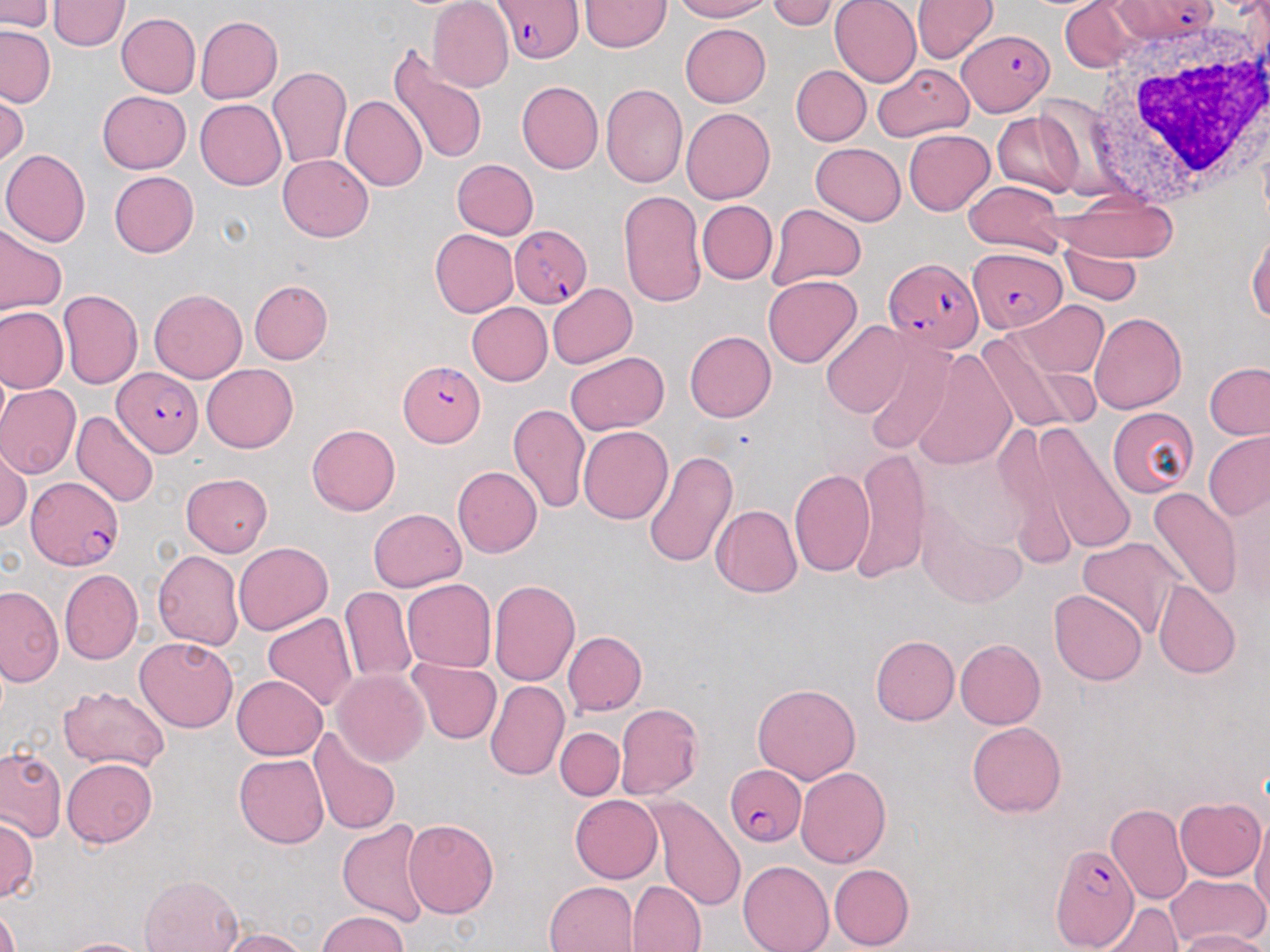
Summary:
  - Coordinate format: approximate bounding boxes as [x1, y1, x2, y2] in pixels
  - Plasmodium falciparum-infected red blood cell locations: [492, 0, 586, 64], [1110, 0, 1219, 42], [958, 29, 1054, 115], [509, 225, 591, 308], [967, 246, 1067, 333], [885, 257, 984, 354], [400, 361, 485, 446], [113, 368, 205, 457], [25, 475, 123, 571], [722, 767, 806, 847], [1049, 845, 1140, 949]
  - White blood cell locations: [1089, 24, 1270, 208]
  - Uninfected red blood cell locations: [428, 0, 513, 92], [579, 0, 669, 52], [671, 0, 775, 21], [767, 0, 838, 30], [830, 0, 922, 87], [911, 0, 999, 63], [1059, 0, 1139, 72], [0, 1, 54, 33], [48, 1, 129, 52], [116, 13, 200, 97], [195, 16, 283, 104], [680, 24, 771, 106], [0, 26, 55, 107], [387, 46, 490, 165], [872, 62, 974, 143], [266, 65, 352, 170], [790, 65, 870, 145], [516, 80, 603, 174], [601, 83, 687, 187], [98, 90, 190, 173], [0, 92, 27, 168], [341, 95, 427, 192], [195, 99, 286, 190], [680, 107, 774, 204], [992, 113, 1082, 196], [904, 129, 995, 215], [811, 143, 905, 225], [1, 150, 91, 247], [278, 154, 373, 242], [452, 159, 539, 239], [109, 171, 199, 258], [964, 181, 1065, 255], [618, 190, 706, 307], [1052, 194, 1176, 262], [697, 200, 777, 284], [767, 203, 867, 289], [0, 225, 66, 316], [1247, 228, 1270, 323], [431, 229, 518, 317], [1062, 244, 1140, 304], [763, 274, 862, 368], [249, 280, 333, 363], [547, 283, 637, 368], [59, 289, 142, 387], [149, 289, 246, 382], [1011, 300, 1107, 378], [467, 303, 553, 386], [0, 306, 68, 393], [1090, 311, 1187, 414], [820, 321, 912, 417], [976, 326, 1094, 437], [685, 331, 777, 422], [859, 334, 956, 455], [912, 348, 1017, 472], [566, 351, 669, 436], [1203, 362, 1270, 440], [201, 364, 298, 453], [0, 385, 81, 479], [507, 403, 590, 514], [1107, 406, 1198, 498], [71, 410, 158, 508], [1022, 421, 1137, 557], [307, 425, 400, 516], [578, 426, 672, 525], [992, 427, 1080, 573], [1203, 431, 1270, 520], [0, 443, 31, 532], [851, 448, 930, 582], [643, 449, 737, 570], [452, 466, 542, 557], [788, 468, 874, 576], [181, 473, 272, 555], [1145, 488, 1242, 602], [914, 498, 1026, 607], [711, 505, 803, 598], [368, 508, 466, 593], [1076, 536, 1187, 641], [233, 542, 332, 634], [152, 549, 244, 650], [59, 568, 142, 665], [402, 578, 497, 673], [489, 580, 579, 686], [1153, 581, 1243, 679], [0, 586, 63, 687], [341, 586, 416, 684], [1049, 589, 1146, 686], [262, 612, 359, 711], [563, 631, 647, 716], [871, 635, 959, 726], [134, 636, 239, 733], [956, 639, 1045, 729], [407, 660, 502, 744], [333, 669, 429, 767], [233, 675, 328, 759], [487, 679, 569, 782], [752, 681, 861, 785], [57, 686, 171, 772], [615, 703, 704, 799], [967, 722, 1066, 818], [309, 727, 401, 834], [555, 727, 624, 799], [0, 746, 65, 841], [234, 754, 329, 848], [62, 758, 157, 847], [796, 768, 892, 868], [570, 795, 663, 883], [644, 796, 748, 913], [1174, 797, 1265, 881], [1106, 804, 1192, 907], [0, 815, 38, 903], [1251, 817, 1270, 920], [403, 818, 499, 918], [337, 819, 431, 927], [738, 860, 834, 952], [829, 863, 914, 951], [1165, 873, 1268, 947], [140, 874, 243, 952], [627, 880, 707, 952], [544, 881, 638, 952], [0, 900, 20, 952], [1097, 901, 1182, 952], [316, 911, 408, 951], [216, 927, 311, 952], [1172, 929, 1267, 952], [58, 937, 154, 952]
  - Slide-level diagnosis: Plasmodium falciparum
  - Modality: optical microscopy
  - Preparation: thin blood film
  - Stain: May-Grünwald-Giemsa
  - Field of view: single
  - Magnification: 1000x
  - Image size: 1270×952 pixels